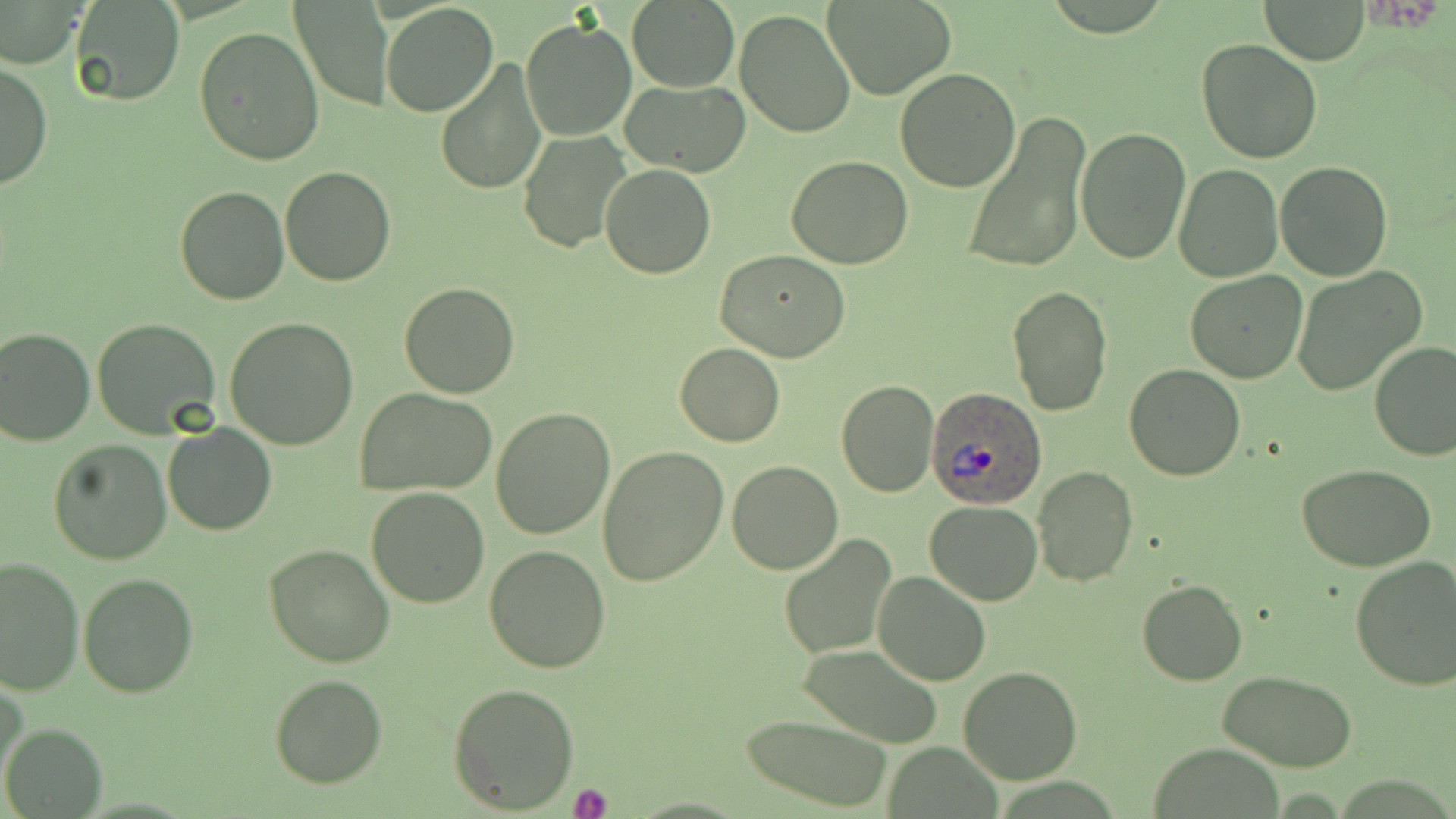

slide-level diagnosis = Plasmodium ovale
image size = 1456×819 pixels
magnification = 1000x
field of view = single
modality = optical microscopy
preparation = thin blood smear
stain = May-Grünwald-Giemsa
platelet locations = approximate bounding boxes as [x1, y1, x2, y2] in pixels: [571, 783, 612, 819]
uninfected red blood cell locations = approximate bounding boxes as [x1, y1, x2, y2] in pixels: [69, 0, 185, 105], [625, 0, 741, 92], [826, 0, 956, 101], [288, 1, 394, 111], [1262, 1, 1370, 64], [380, 2, 499, 118], [0, 3, 86, 69], [733, 9, 856, 139], [518, 18, 637, 142], [194, 26, 327, 165], [1195, 38, 1323, 164], [435, 59, 548, 193], [1, 61, 52, 193], [894, 68, 1021, 192], [619, 79, 751, 178], [961, 114, 1091, 274], [1075, 127, 1191, 264], [518, 129, 634, 254], [787, 156, 914, 269], [1275, 161, 1394, 281], [279, 164, 396, 285], [601, 164, 716, 279], [1173, 164, 1282, 282], [173, 185, 290, 305], [714, 249, 851, 363], [1292, 266, 1428, 397], [1185, 270, 1307, 383], [399, 283, 519, 399], [1007, 286, 1113, 416], [91, 317, 222, 439], [224, 317, 359, 450], [0, 326, 95, 446], [1369, 341, 1456, 460], [675, 343, 784, 447], [1124, 364, 1248, 481], [835, 380, 939, 497], [357, 388, 498, 495], [491, 407, 615, 539], [163, 422, 276, 536], [48, 439, 172, 565], [597, 443, 729, 587], [726, 461, 843, 575], [1296, 464, 1437, 572], [1032, 466, 1138, 587], [366, 487, 490, 607], [923, 500, 1045, 603], [777, 532, 897, 660], [264, 543, 396, 668], [483, 545, 611, 673], [0, 555, 84, 698], [1350, 556, 1456, 691], [873, 571, 991, 686], [78, 573, 198, 698], [1137, 580, 1247, 686], [796, 643, 945, 747], [958, 667, 1083, 784], [1219, 670, 1358, 771], [269, 675, 387, 789], [1, 677, 26, 791], [448, 682, 580, 814], [743, 716, 894, 812], [1, 722, 107, 817], [1148, 742, 1286, 818]
Plasmodium ovale-infected red blood cell locations = approximate bounding boxes as [x1, y1, x2, y2] in pixels: [926, 388, 1049, 508]